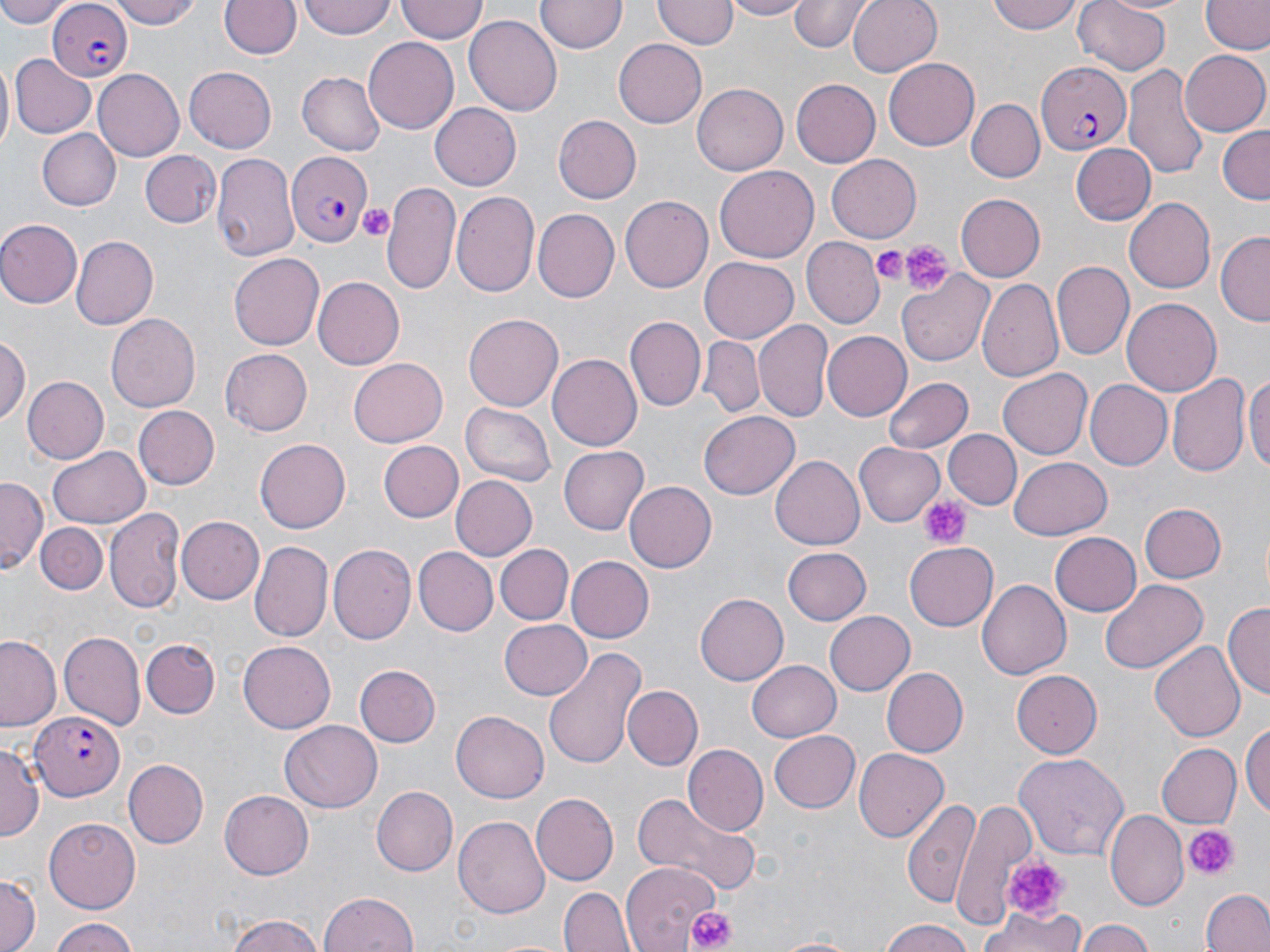

Approximate bounding boxes as (x1, y1, x2, y2) in pixels. Platelet locations: (356, 202, 394, 243), (899, 239, 953, 295), (872, 245, 910, 284), (919, 494, 973, 550), (1182, 823, 1239, 882), (1000, 855, 1068, 920), (673, 904, 743, 950). Uninfected red blood cell locations: (3, 0, 68, 29), (113, 0, 203, 28), (219, 0, 302, 60), (299, 0, 398, 39), (396, 0, 486, 43), (537, 0, 626, 54), (654, 0, 734, 50), (724, 0, 812, 20), (789, 0, 874, 52), (847, 0, 943, 77), (988, 0, 1085, 35), (1073, 0, 1171, 75), (1203, 1, 1269, 56), (1194, 2, 1270, 115), (465, 16, 563, 115), (363, 36, 461, 134), (615, 39, 707, 128), (1180, 50, 1268, 136), (12, 53, 96, 138), (882, 58, 979, 151), (0, 59, 13, 157), (184, 64, 276, 150), (1125, 64, 1211, 184), (92, 69, 184, 161), (297, 73, 386, 156), (789, 79, 879, 168), (692, 82, 787, 174), (967, 97, 1045, 180), (430, 103, 521, 190), (552, 115, 641, 204), (1218, 125, 1270, 204), (37, 129, 120, 210), (1071, 144, 1156, 225), (139, 148, 220, 227), (213, 153, 297, 262), (828, 154, 924, 242), (715, 166, 819, 262), (382, 179, 464, 295), (451, 190, 540, 296), (622, 194, 716, 293), (955, 194, 1045, 280), (1124, 197, 1215, 293), (534, 209, 618, 301), (0, 218, 82, 309), (1217, 232, 1270, 327), (71, 236, 158, 330), (803, 239, 881, 329), (230, 251, 323, 347), (700, 258, 798, 342), (1051, 262, 1133, 361), (900, 272, 994, 366), (979, 276, 1063, 383), (314, 277, 404, 367), (1120, 298, 1221, 397), (464, 313, 563, 413), (105, 314, 200, 413), (626, 316, 705, 410), (756, 319, 833, 421), (820, 331, 911, 422), (0, 336, 28, 428), (698, 337, 763, 417), (218, 349, 312, 436), (548, 354, 641, 450), (347, 356, 447, 446), (998, 369, 1093, 458), (1245, 369, 1270, 482), (1167, 371, 1249, 478), (25, 376, 109, 464), (884, 376, 973, 454), (1087, 380, 1173, 469), (461, 401, 554, 486), (135, 407, 219, 488), (699, 412, 800, 498), (944, 429, 1021, 509), (257, 438, 353, 533), (377, 440, 464, 522), (855, 443, 943, 526), (47, 446, 150, 529), (560, 448, 648, 534), (770, 455, 863, 551), (1009, 457, 1112, 540), (0, 475, 47, 569), (452, 475, 538, 560), (625, 482, 716, 572), (1139, 502, 1227, 583), (106, 506, 184, 612), (178, 517, 264, 604), (36, 522, 107, 595), (1051, 532, 1142, 616), (249, 543, 331, 643), (495, 543, 572, 622), (328, 544, 415, 648), (905, 544, 998, 629), (781, 547, 872, 625), (413, 548, 495, 636), (420, 551, 577, 629), (565, 556, 653, 643), (977, 579, 1070, 681), (1099, 579, 1208, 676), (695, 594, 787, 685), (1224, 599, 1270, 698), (825, 612, 915, 695), (499, 619, 592, 700), (57, 627, 145, 728), (0, 636, 62, 733), (142, 637, 220, 718), (1151, 641, 1245, 745), (237, 642, 336, 733), (540, 644, 645, 770), (748, 659, 840, 742), (356, 665, 439, 746), (882, 667, 969, 757), (1010, 671, 1101, 758), (621, 685, 701, 771), (450, 711, 548, 802), (281, 719, 383, 812), (1242, 720, 1270, 819), (768, 730, 861, 813), (0, 740, 42, 846), (1155, 743, 1240, 831), (681, 744, 767, 836), (854, 748, 949, 841), (1012, 751, 1130, 860), (122, 757, 209, 849), (373, 784, 460, 876), (219, 789, 312, 879), (628, 792, 761, 900), (900, 793, 981, 907), (531, 794, 619, 885), (953, 801, 1042, 928), (1106, 811, 1188, 909), (455, 816, 550, 920), (43, 818, 140, 911), (620, 860, 722, 949), (0, 872, 39, 952), (559, 886, 634, 952), (1203, 887, 1270, 952), (320, 890, 419, 952), (981, 905, 1084, 952), (222, 914, 330, 952), (46, 916, 140, 951), (1076, 919, 1156, 952), (876, 921, 980, 952), (768, 934, 868, 951). Plasmodium falciparum-infected red blood cell locations: (45, 1, 131, 81), (1035, 59, 1132, 155), (282, 149, 371, 248), (28, 713, 123, 799). Slide-level diagnosis: Plasmodium falciparum. Thin blood smear. Single field of view. Light microscopy. Image is 1270×952 pixels. May-Grünwald-Giemsa stain. 1000x magnification.